State the blood parasite species.
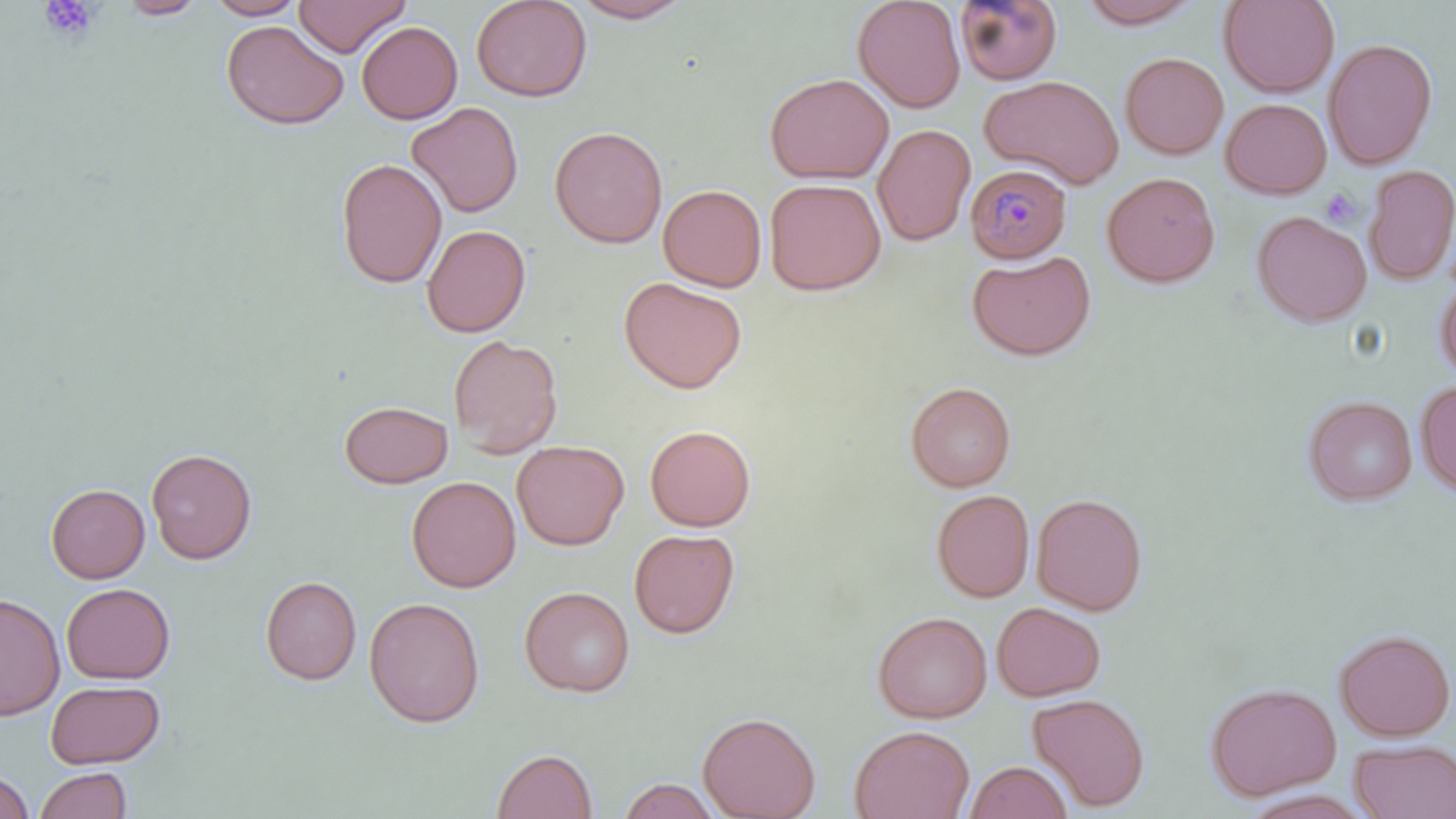

Plasmodium malariae.

Approximate bounding boxes as (x1,y1)-(x2,y2) corner pairs in pixels. Platelet locations: (38,0)-(101,41), (1321,188)-(1362,228). Uninfected red blood cell locations: (115,0)-(208,19), (205,0)-(308,20), (293,0)-(410,57), (471,0)-(593,102), (570,0)-(695,23), (852,0)-(965,112), (954,0)-(1063,85), (1077,0)-(1204,29), (1219,0)-(1340,97), (221,19)-(349,130), (357,21)-(463,124), (1323,38)-(1438,169), (1120,52)-(1229,159), (764,72)-(894,184), (980,74)-(1123,189), (1220,98)-(1332,199), (406,101)-(524,218), (873,123)-(976,246), (549,125)-(668,249), (335,158)-(448,289), (1364,165)-(1456,286), (1102,171)-(1221,288), (764,178)-(886,295), (658,184)-(767,292), (1252,210)-(1372,328), (421,224)-(531,337), (966,249)-(1096,361), (1434,273)-(1456,384), (618,277)-(747,394), (448,334)-(563,458), (1415,379)-(1456,497), (905,382)-(1016,492), (1304,395)-(1418,505), (339,400)-(453,489), (645,425)-(756,531), (512,440)-(629,550), (146,447)-(257,564), (406,476)-(521,593), (46,483)-(150,584), (931,489)-(1034,602), (1031,492)-(1147,615), (629,528)-(740,639), (260,575)-(362,685), (62,582)-(175,684), (519,586)-(635,698), (0,592)-(65,721), (364,596)-(485,728), (992,602)-(1106,701), (872,611)-(992,724), (1334,628)-(1455,742), (46,679)-(165,769), (1205,682)-(1341,800), (1027,693)-(1150,811), (698,711)-(821,819), (848,724)-(975,819), (1349,739)-(1456,819), (492,749)-(598,819), (964,760)-(1072,819), (34,767)-(133,819), (1,768)-(35,818), (618,777)-(721,819). Plasmodium malariae-infected red blood cell locations: (965,163)-(1072,263). Thin blood smear. Image is 1456×819 pixels. Single field of view. 1000x magnification. Light microscopy. May-Grünwald-Giemsa stain.